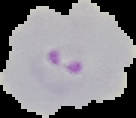
Summary:
  - Result: malaria parasites detected
  - Preparation: thin blood smear
  - Image size: 136×118 pixels
  - Image type: segmented cell region on a black background